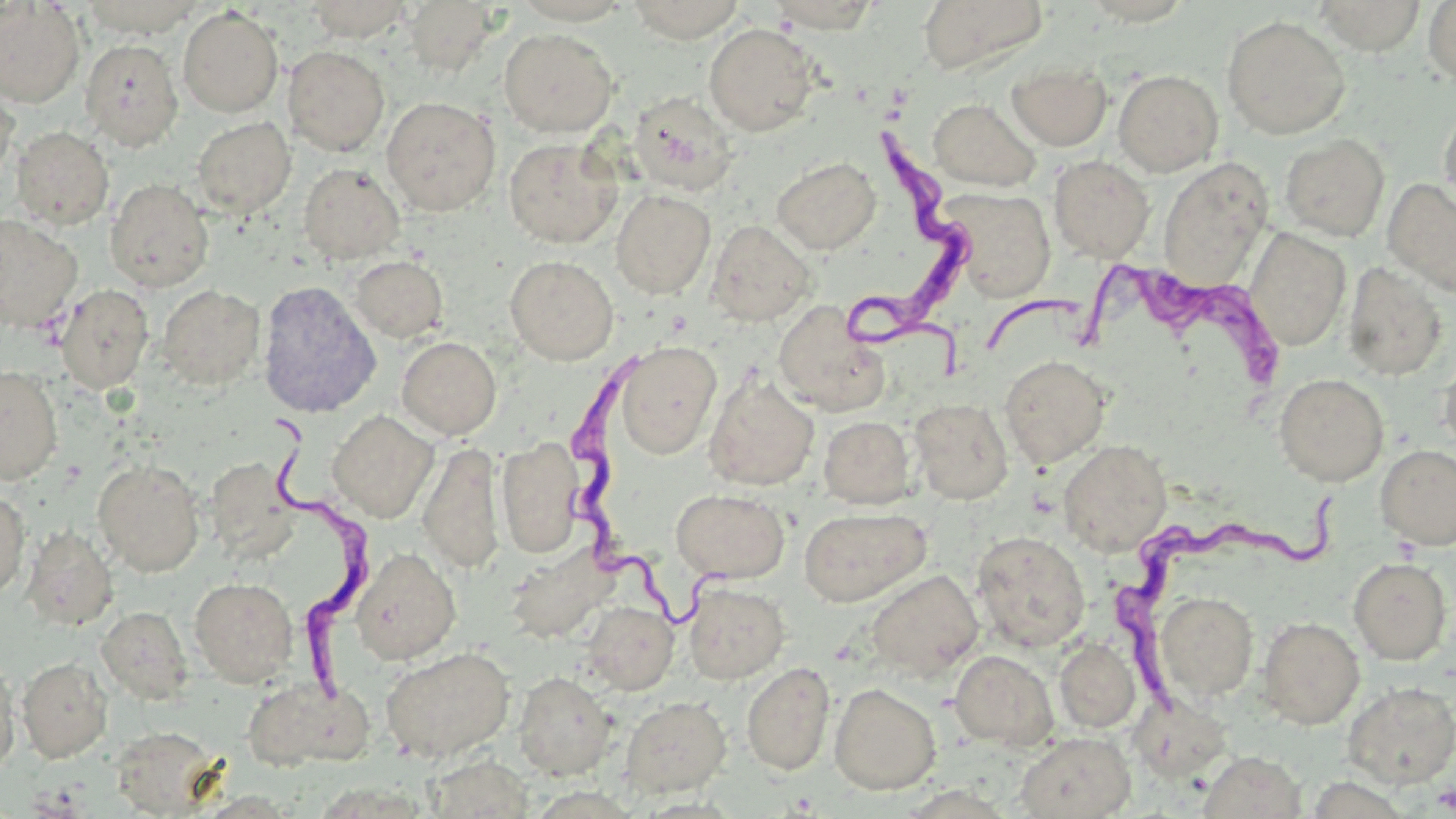

Summary:
  - Coordinate format: approximate bounding boxes as (x1, y1, x2, y2) in pixels
  - Trypanosoma brucei locations: (838, 124, 967, 375), (1081, 262, 1284, 395), (560, 355, 733, 629), (263, 424, 381, 708), (1113, 490, 1345, 725)
  - Uninfected red blood cell locations: (80, 0, 206, 37), (304, 0, 415, 41), (626, 0, 746, 42), (768, 0, 882, 32), (918, 0, 1048, 75), (1314, 0, 1427, 55), (0, 1, 85, 108), (404, 1, 499, 76), (1079, 1, 1196, 26), (1423, 1, 1456, 87), (178, 6, 284, 117), (1222, 15, 1350, 139), (704, 23, 819, 136), (498, 28, 619, 137), (79, 39, 184, 151), (283, 46, 390, 156), (1007, 61, 1111, 150), (1113, 69, 1224, 176), (0, 88, 18, 189), (627, 92, 738, 196), (381, 96, 501, 216), (928, 98, 1041, 191), (1439, 103, 1456, 219), (192, 116, 296, 218), (11, 125, 114, 230), (1279, 134, 1390, 241), (503, 138, 622, 248), (1049, 155, 1155, 263), (771, 157, 881, 254), (1158, 158, 1273, 289), (298, 163, 406, 265), (105, 178, 214, 292), (1382, 178, 1456, 297), (940, 187, 1057, 302), (611, 189, 716, 299), (0, 214, 83, 333), (706, 220, 816, 327), (1245, 227, 1351, 351), (350, 255, 448, 343), (505, 255, 619, 365), (1342, 261, 1448, 381), (257, 279, 381, 418), (55, 284, 154, 394), (157, 284, 265, 390), (773, 300, 889, 416), (397, 336, 501, 439), (615, 342, 721, 459), (1438, 351, 1456, 457), (1000, 355, 1111, 468), (0, 365, 63, 485), (704, 372, 819, 491), (1274, 373, 1389, 485), (909, 398, 1013, 505), (327, 410, 439, 522), (819, 416, 916, 508), (496, 437, 585, 558), (1059, 439, 1172, 557), (418, 442, 505, 574), (1375, 445, 1456, 550), (204, 457, 300, 561), (93, 459, 205, 576), (671, 488, 790, 583), (0, 490, 30, 599), (798, 507, 930, 606), (21, 527, 118, 630), (971, 531, 1090, 653), (503, 543, 617, 643), (350, 547, 461, 665), (1348, 557, 1452, 664), (866, 569, 984, 680), (189, 577, 298, 686), (683, 581, 789, 684), (1154, 591, 1259, 702), (582, 597, 791, 692), (95, 599, 300, 699), (583, 601, 678, 694), (97, 606, 193, 703), (1257, 616, 1365, 729), (1054, 638, 1140, 732), (380, 646, 515, 762), (949, 650, 1058, 749), (17, 656, 112, 763), (0, 657, 19, 780), (742, 661, 835, 776), (513, 671, 616, 780), (240, 678, 367, 771), (1343, 681, 1456, 788), (829, 682, 942, 795), (1128, 692, 1232, 782), (619, 696, 731, 798), (109, 729, 225, 816), (1016, 731, 1135, 819), (1198, 750, 1306, 819)
  - Slide-level diagnosis: Trypanosoma brucei
  - Stain: May-Grünwald-Giemsa
  - Preparation: thin blood smear
  - Modality: light microscopy
  - Field of view: single
  - Image size: 1456×819 pixels
  - Magnification: 1000x